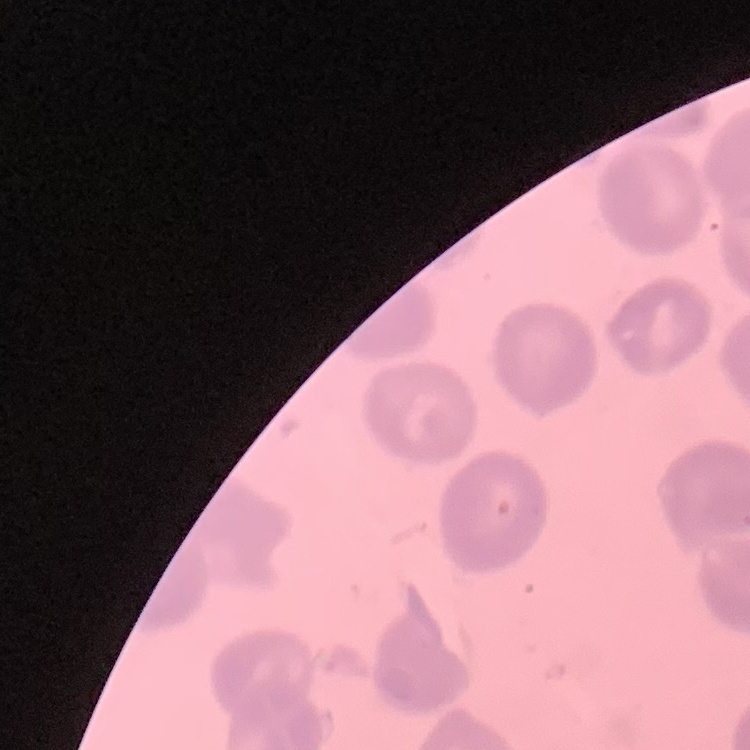
red blood cell morphology = no rouleaux formation
image type = square crop of a larger photomicrograph
preparation = thin blood film
stain = Field's or Giemsa